Identify the parasite.
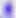
Toxoplasma gondii.

Summary:
  - Modality: photomicrograph
  - Magnification: 400x